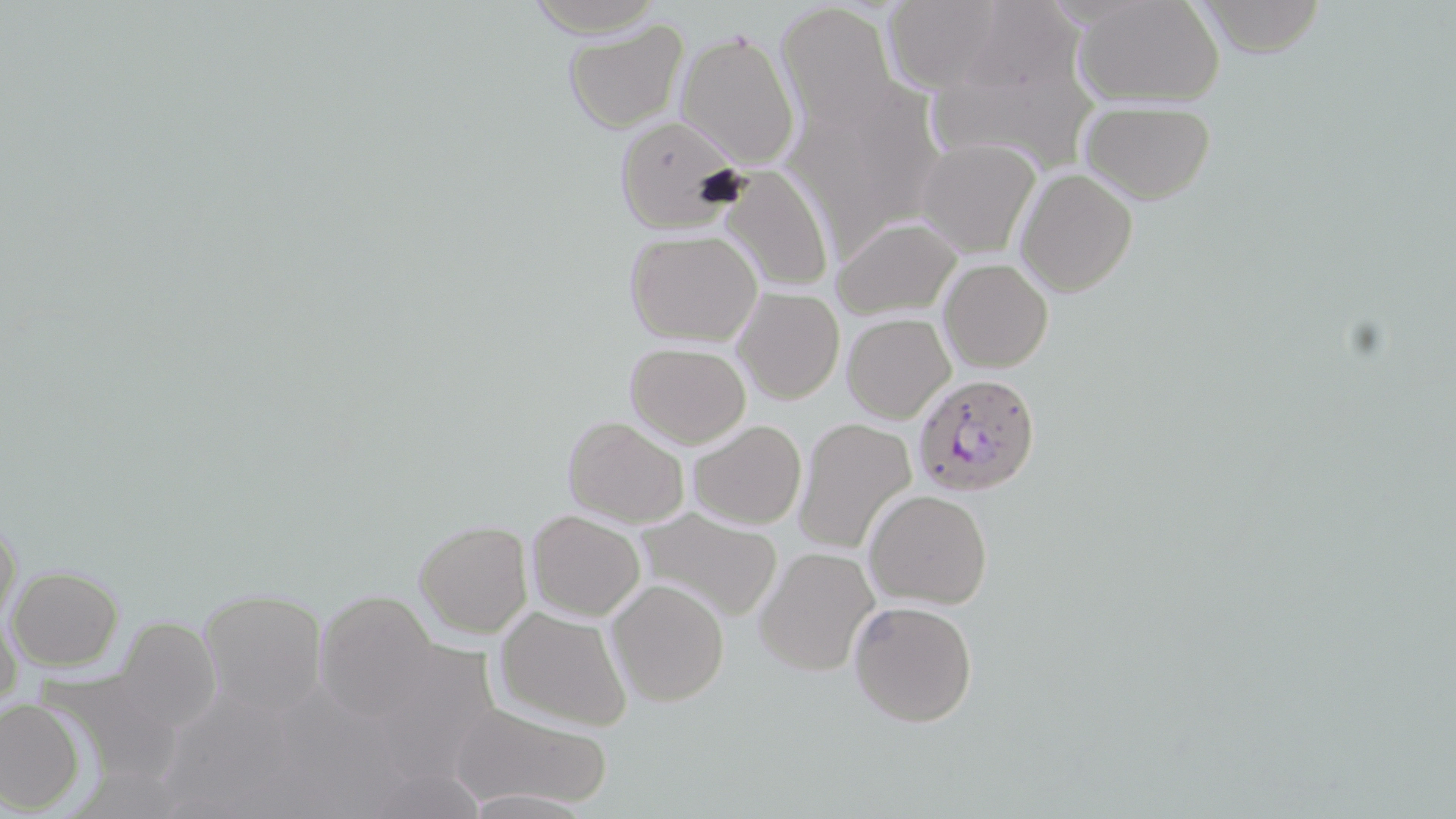

Approximate bounding boxes as [x1, y1, x2, y2] in pixels. Plasmodium falciparum-infected red blood cell locations: [910, 375, 1041, 498]. Uninfected red blood cell locations: [881, 0, 1018, 94], [1077, 0, 1225, 106], [1196, 0, 1330, 57], [521, 1, 665, 36], [777, 2, 902, 129], [563, 18, 690, 134], [674, 28, 801, 169], [783, 74, 944, 253], [1077, 95, 1216, 204], [612, 116, 748, 231], [915, 140, 1039, 257], [720, 165, 835, 294], [1016, 168, 1137, 296], [833, 215, 961, 320], [625, 228, 762, 346], [938, 259, 1053, 372], [733, 287, 844, 404], [843, 313, 954, 424], [624, 343, 751, 449], [562, 414, 689, 528], [794, 416, 917, 554], [687, 419, 807, 531], [865, 490, 992, 608], [632, 507, 786, 623], [526, 509, 646, 622], [1, 511, 22, 632], [413, 519, 532, 638], [754, 546, 880, 677], [7, 565, 123, 669], [606, 580, 729, 706], [200, 588, 328, 713], [311, 590, 445, 720], [848, 598, 979, 728], [496, 606, 633, 731], [1, 614, 22, 701], [112, 617, 223, 735], [0, 697, 85, 814], [451, 702, 609, 810]. Slide-level diagnosis: Plasmodium falciparum. Thin blood film. 1000x magnification. Optical microscopy. Image is 1456×819 pixels. One field of a larger specimen. May-Grünwald-Giemsa-stained preparation.